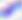

Summary:
  - Magnification: 400x
  - Modality: photomicrograph
  - Identification: Toxoplasma gondii